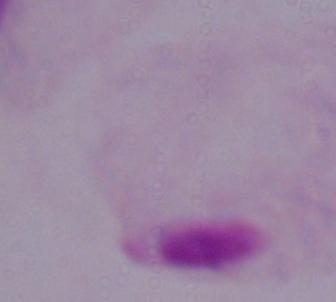
{
  "magnification": "1000x",
  "identification": "trichomonad",
  "modality": "micrograph"
}